Draw a bounding box around every malaria parasite.
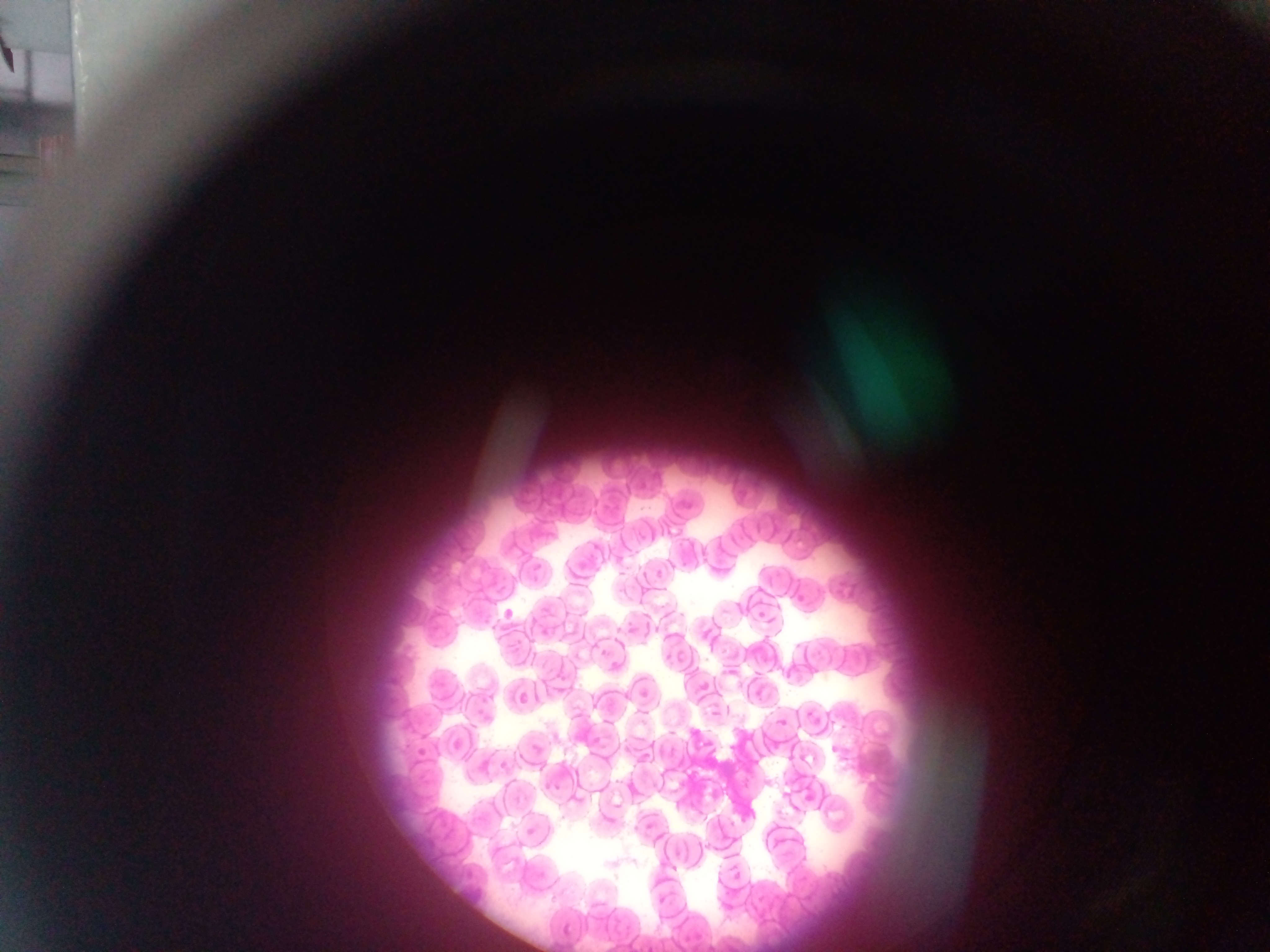

Approximate bounding boxes as (left, top, right, bottom) in pixels.
Malaria parasites: (529, 548, 555, 571), (577, 554, 591, 567), (679, 555, 696, 570), (650, 562, 671, 579), (795, 586, 814, 608), (504, 600, 515, 621), (757, 609, 770, 617), (594, 646, 613, 662), (694, 675, 716, 693), (751, 683, 769, 695), (637, 687, 652, 698), (520, 694, 530, 704), (806, 711, 827, 728), (776, 712, 794, 729), (591, 734, 604, 743), (447, 737, 463, 757), (826, 739, 841, 757), (527, 741, 539, 756), (416, 745, 434, 757), (498, 756, 515, 775), (543, 777, 559, 792), (800, 784, 814, 805), (524, 815, 547, 835), (442, 823, 459, 843), (729, 864, 748, 882), (560, 922, 573, 935).

Summary:
  - Field of view: single
  - Preparation: thin blood smear
  - Capture: mobile-phone photograph through a microscope
  - Image size: 1270×952 pixels
  - Country: Ghana